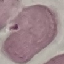

Malaria status: uninfected. Thin blood film. Acquired by smartphone through the microscope eyepiece. Giemsa-stained preparation. Cell patch, automatically extracted from a larger field of view and resized to 64 × 64 pixels.